Describe the morphology of the erythrocytes.
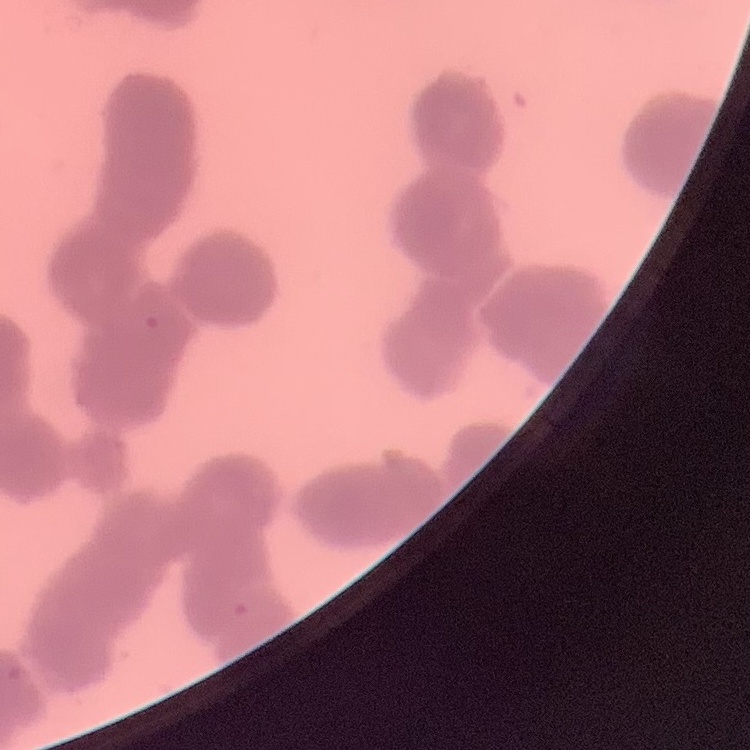

Rouleaux formation.

Field's or Giemsa stain. Thin blood film. One tile cut from a larger photomicrograph.